Assess this cell for malaria.
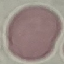

Uninfected.

preparation = thin blood film
stain = Giemsa
capture = smartphone through the microscope eyepiece
image type = automatically extracted cell patch, resized to 64 × 64 pixels